Name the parasite shown.
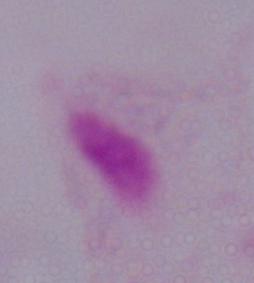

This is a trichomonad.

1000x magnification. Micrograph.